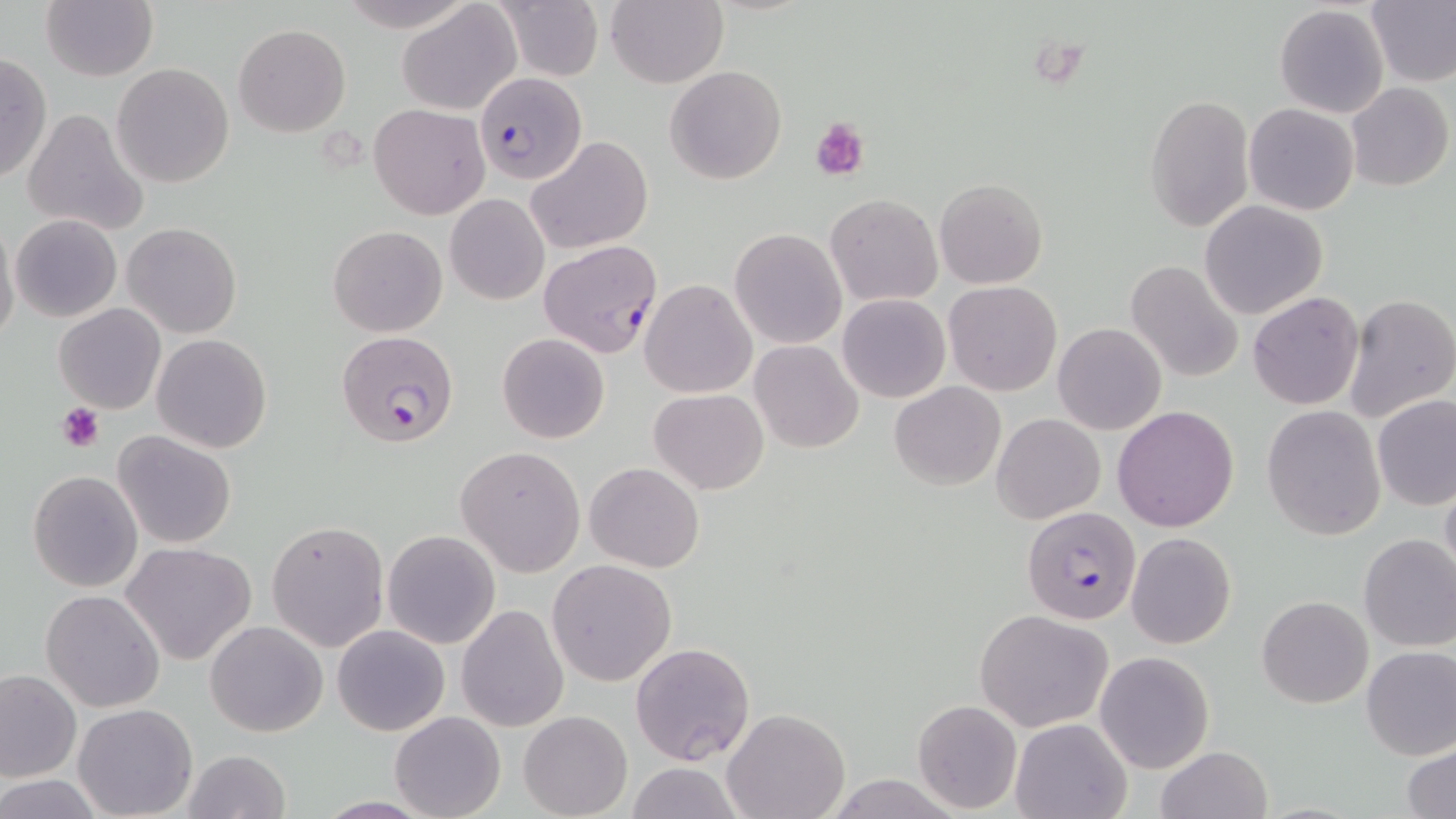

slide-level diagnosis = Plasmodium falciparum
stain = May-Grünwald-Giemsa
modality = optical microscopy
magnification = 1000x
image size = 1456×819 pixels
preparation = thin blood smear
uninfected red blood cell locations = approximate bounding boxes as [x1, y1, x2, y2] in pixels: [337, 0, 477, 30], [493, 0, 604, 81], [606, 0, 727, 89], [1365, 0, 1456, 88], [396, 1, 521, 116], [42, 2, 156, 82], [1274, 4, 1390, 118], [233, 24, 351, 136], [0, 52, 51, 187], [111, 63, 235, 187], [665, 65, 785, 184], [1346, 83, 1454, 192], [1144, 92, 1253, 233], [369, 104, 489, 219], [1245, 104, 1360, 215], [22, 107, 148, 238], [526, 135, 654, 255], [935, 178, 1047, 288], [445, 194, 549, 305], [825, 194, 943, 307], [1200, 200, 1328, 319], [11, 214, 122, 323], [0, 219, 20, 348], [121, 222, 242, 338], [328, 225, 447, 337], [729, 228, 848, 349], [1125, 259, 1245, 383], [640, 279, 758, 399], [943, 281, 1061, 395], [1248, 292, 1364, 409], [1344, 293, 1456, 423], [837, 294, 950, 404], [55, 302, 166, 414], [1052, 322, 1168, 434], [497, 333, 610, 443], [152, 334, 272, 454], [750, 340, 863, 453], [890, 381, 1005, 490], [649, 388, 767, 495], [1372, 394, 1455, 510], [899, 401, 1111, 511], [1261, 404, 1386, 541], [1112, 406, 1240, 531], [993, 414, 1106, 523], [113, 431, 237, 549], [456, 445, 585, 577], [585, 462, 704, 572], [28, 471, 142, 592], [1439, 473, 1456, 589], [265, 519, 389, 653], [381, 529, 501, 650], [1126, 533, 1236, 648], [1358, 533, 1456, 653], [121, 541, 257, 664], [547, 558, 677, 687], [41, 590, 166, 712], [1257, 595, 1371, 708], [457, 603, 570, 732], [975, 609, 1113, 732], [204, 621, 328, 736], [332, 623, 450, 736], [630, 642, 756, 765], [1360, 646, 1456, 760], [1095, 651, 1214, 773], [1, 669, 80, 782], [912, 699, 1022, 814], [73, 703, 199, 818], [390, 709, 506, 819], [723, 709, 850, 819], [519, 710, 631, 818], [1010, 717, 1130, 819], [1404, 742, 1456, 818], [1157, 745, 1272, 819], [181, 749, 291, 819], [621, 763, 744, 819], [0, 775, 106, 816]
platelet locations = approximate bounding boxes as [x1, y1, x2, y2] in pixels: [811, 118, 867, 180], [57, 403, 106, 451]
field of view = one of a larger specimen
Plasmodium falciparum-infected red blood cell locations = approximate bounding boxes as [x1, y1, x2, y2] in pixels: [475, 72, 586, 185], [539, 241, 662, 358], [334, 330, 460, 447], [1023, 506, 1141, 624]